Name the cell type shown.
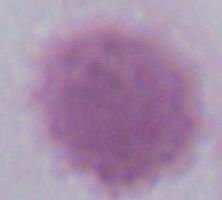

An erythrocyte.

modality = photomicrograph
magnification = 1000x